Locate every blood parasite and identify its species.
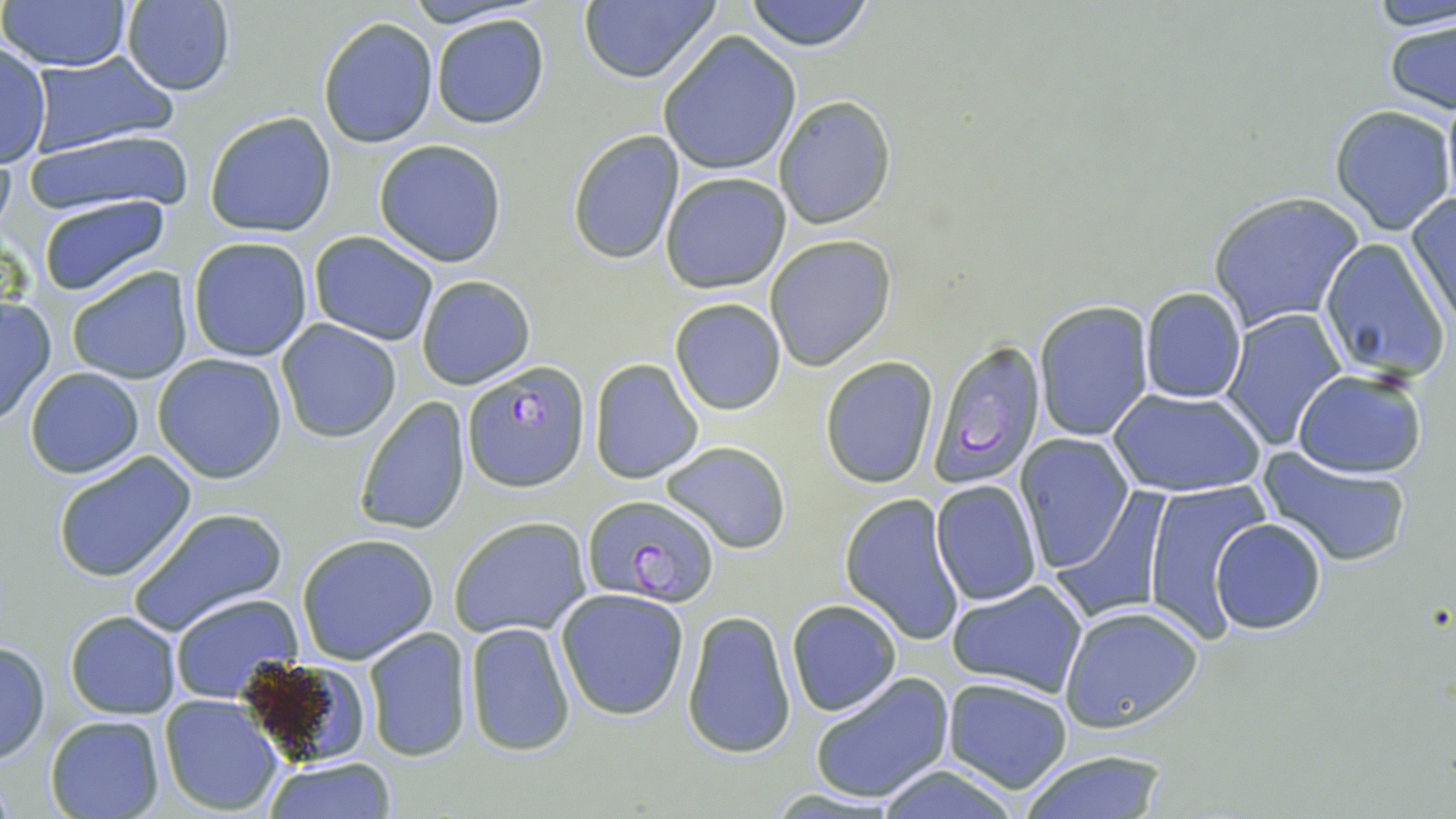

Approximate bounding boxes as named x1/y1/x2/y2 corners in pixels.
Plasmodium falciparum-infected red blood cells: (x1=926, y1=338, x2=1045, y2=488), (x1=461, y1=360, x2=589, y2=493), (x1=583, y1=492, x2=718, y2=605).
No Plasmodium ovale, Plasmodium malariae, Plasmodium vivax, Babesia divergens, or Trypanosoma brucei observed.

Summary:
  - Uninfected red blood cell locations: (x1=2, y1=0, x2=134, y2=73), (x1=575, y1=0, x2=722, y2=86), (x1=741, y1=0, x2=878, y2=52), (x1=1362, y1=0, x2=1455, y2=35), (x1=118, y1=2, x2=236, y2=96), (x1=431, y1=14, x2=550, y2=130), (x1=1382, y1=16, x2=1456, y2=116), (x1=318, y1=17, x2=438, y2=148), (x1=657, y1=31, x2=801, y2=176), (x1=0, y1=40, x2=51, y2=169), (x1=29, y1=51, x2=177, y2=155), (x1=1439, y1=90, x2=1455, y2=220), (x1=773, y1=96, x2=895, y2=229), (x1=1328, y1=105, x2=1454, y2=234), (x1=205, y1=111, x2=337, y2=238), (x1=22, y1=128, x2=192, y2=216), (x1=566, y1=131, x2=685, y2=263), (x1=372, y1=139, x2=509, y2=267), (x1=661, y1=171, x2=791, y2=294), (x1=1205, y1=191, x2=1364, y2=334), (x1=36, y1=194, x2=171, y2=296), (x1=1404, y1=194, x2=1456, y2=331), (x1=307, y1=231, x2=438, y2=345), (x1=764, y1=235, x2=896, y2=370), (x1=187, y1=236, x2=315, y2=362), (x1=1318, y1=237, x2=1450, y2=385), (x1=65, y1=266, x2=194, y2=384), (x1=416, y1=274, x2=535, y2=390), (x1=1140, y1=286, x2=1247, y2=403), (x1=0, y1=295, x2=55, y2=426), (x1=670, y1=298, x2=786, y2=415), (x1=1032, y1=300, x2=1153, y2=441), (x1=1221, y1=310, x2=1345, y2=449), (x1=277, y1=320, x2=401, y2=442), (x1=153, y1=353, x2=289, y2=483), (x1=819, y1=356, x2=939, y2=489), (x1=588, y1=359, x2=703, y2=484), (x1=24, y1=367, x2=144, y2=477), (x1=1292, y1=368, x2=1428, y2=477), (x1=1108, y1=387, x2=1267, y2=497), (x1=353, y1=397, x2=473, y2=535), (x1=1016, y1=435, x2=1134, y2=573), (x1=660, y1=440, x2=792, y2=554), (x1=51, y1=449, x2=197, y2=584), (x1=1257, y1=450, x2=1412, y2=568), (x1=932, y1=479, x2=1042, y2=607), (x1=1143, y1=485, x2=1268, y2=639), (x1=839, y1=493, x2=965, y2=644), (x1=1054, y1=494, x2=1171, y2=623), (x1=128, y1=506, x2=288, y2=636), (x1=448, y1=516, x2=592, y2=639), (x1=1210, y1=519, x2=1328, y2=634), (x1=295, y1=533, x2=442, y2=663), (x1=947, y1=579, x2=1088, y2=697), (x1=555, y1=588, x2=691, y2=722), (x1=171, y1=593, x2=302, y2=704), (x1=786, y1=599, x2=901, y2=716), (x1=1060, y1=603, x2=1205, y2=732), (x1=682, y1=610, x2=796, y2=759), (x1=64, y1=611, x2=181, y2=719), (x1=464, y1=622, x2=575, y2=758), (x1=363, y1=627, x2=473, y2=761), (x1=0, y1=640, x2=50, y2=765), (x1=236, y1=657, x2=376, y2=764), (x1=808, y1=672, x2=956, y2=805), (x1=941, y1=677, x2=1073, y2=792), (x1=158, y1=695, x2=284, y2=816), (x1=44, y1=716, x2=164, y2=819), (x1=1013, y1=748, x2=1174, y2=819), (x1=261, y1=757, x2=396, y2=818), (x1=870, y1=766, x2=1026, y2=819)
  - Slide-level diagnosis: Plasmodium falciparum
  - Stain: May-Grünwald-Giemsa
  - Magnification: 1000x
  - Field of view: one of a larger specimen
  - Image size: 1456×819 pixels
  - Modality: optical microscopy
  - Preparation: thin blood smear